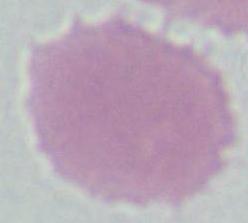
identification = red blood cell
modality = photomicrograph
magnification = 1000x